Report the malaria status of this cell.
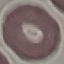

Uninfected.

Giemsa-stained preparation. Thin blood film. Acquired by smartphone through the microscope eyepiece. Cell patch, automatically extracted from a larger field of view and resized to 64 × 64 pixels.